Classify this cell by malaria status.
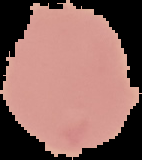
It is uninfected.

preparation: thin blood film
image_size: 142×160 pixels
image_type: segmented cell region with the area outside set to black